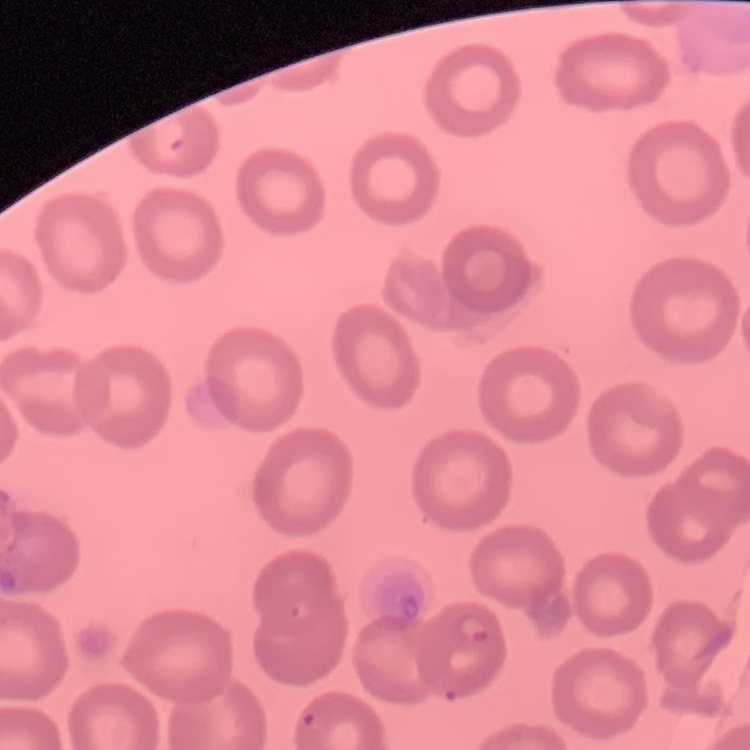

Summary:
  - Erythrocyte morphology: no rouleaux formation
  - Preparation: thin blood smear
  - Stain: Field's or Giemsa
  - Image type: square crop of a larger photomicrograph